Classify this cell by malaria status.
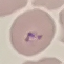

It is parasitized.

Summary:
  - Image type: automatically extracted cell patch, resized to 64 × 64 pixels
  - Stain: Giemsa
  - Capture: smartphone through the microscope eyepiece
  - Preparation: thin smear